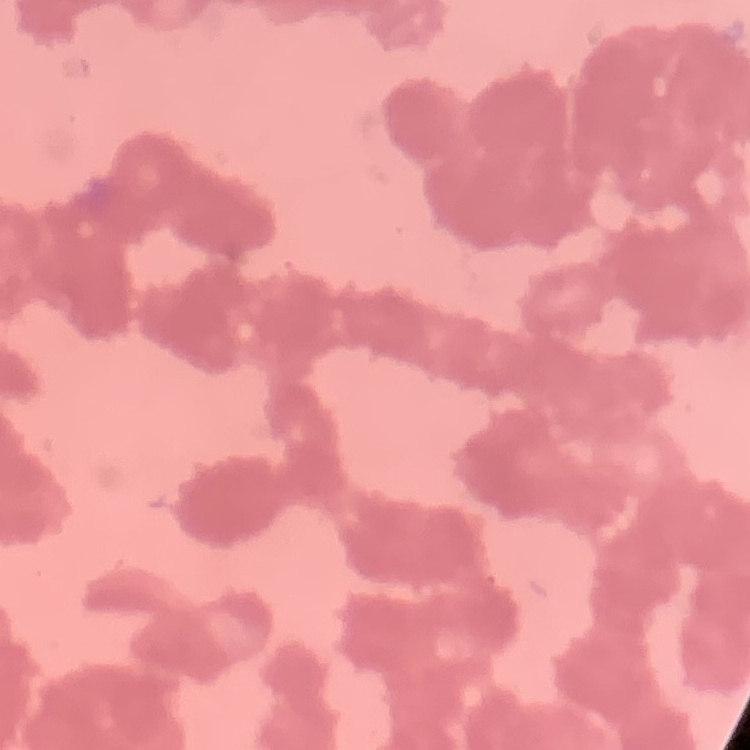
Summary:
  - Red blood cell morphology: rouleaux formation
  - Stain: Field's or Giemsa
  - Image type: one tile cut from a larger photomicrograph
  - Preparation: thin peripheral smear